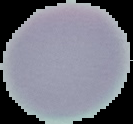
Summary:
  - Malaria status: uninfected
  - Preparation: thin blood smear
  - Image type: segmented cell region with the area outside set to black
  - Image size: 133×124 pixels